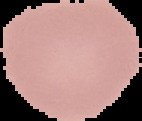

Summary:
  - Image type: segmented cell region on a black background
  - Malaria status: uninfected
  - Image size: 142×121 pixels
  - Preparation: thin blood film